Report the malaria status of this cell.
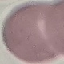

It is uninfected.

Thin blood film. Cell patch, automatically extracted from a larger field of view and resized to 64 × 64 pixels. Giemsa-stained preparation. Acquired by smartphone through the microscope eyepiece.